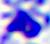

{
  "magnification": "400x",
  "identification": "white blood cell",
  "modality": "micrograph"
}